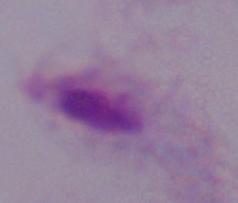
A trichomonad is shown. 1000x magnification. Micrograph.